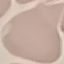 Malaria status: uninfected. Cell patch, automatically extracted from a larger field of view and resized to 64 × 64 pixels. Thin blood film. Acquired by smartphone through the microscope eyepiece. Giemsa stain.